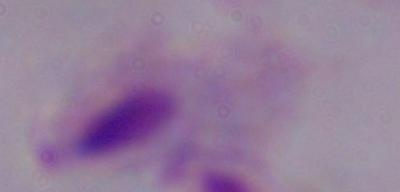

Summary:
  - Identification: trichomonad
  - Magnification: 1000x
  - Modality: micrograph